Classify this cell by malaria status.
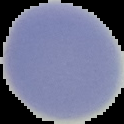
Uninfected.

From a thin blood film. Image is 124×124 pixels. Segmented cell region on a black background.